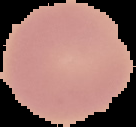
{
  "image_type": "segmented cell region on a black background",
  "preparation": "thin blood film",
  "image_size": "136×127 pixels",
  "result": "negative for Plasmodium parasites"
}